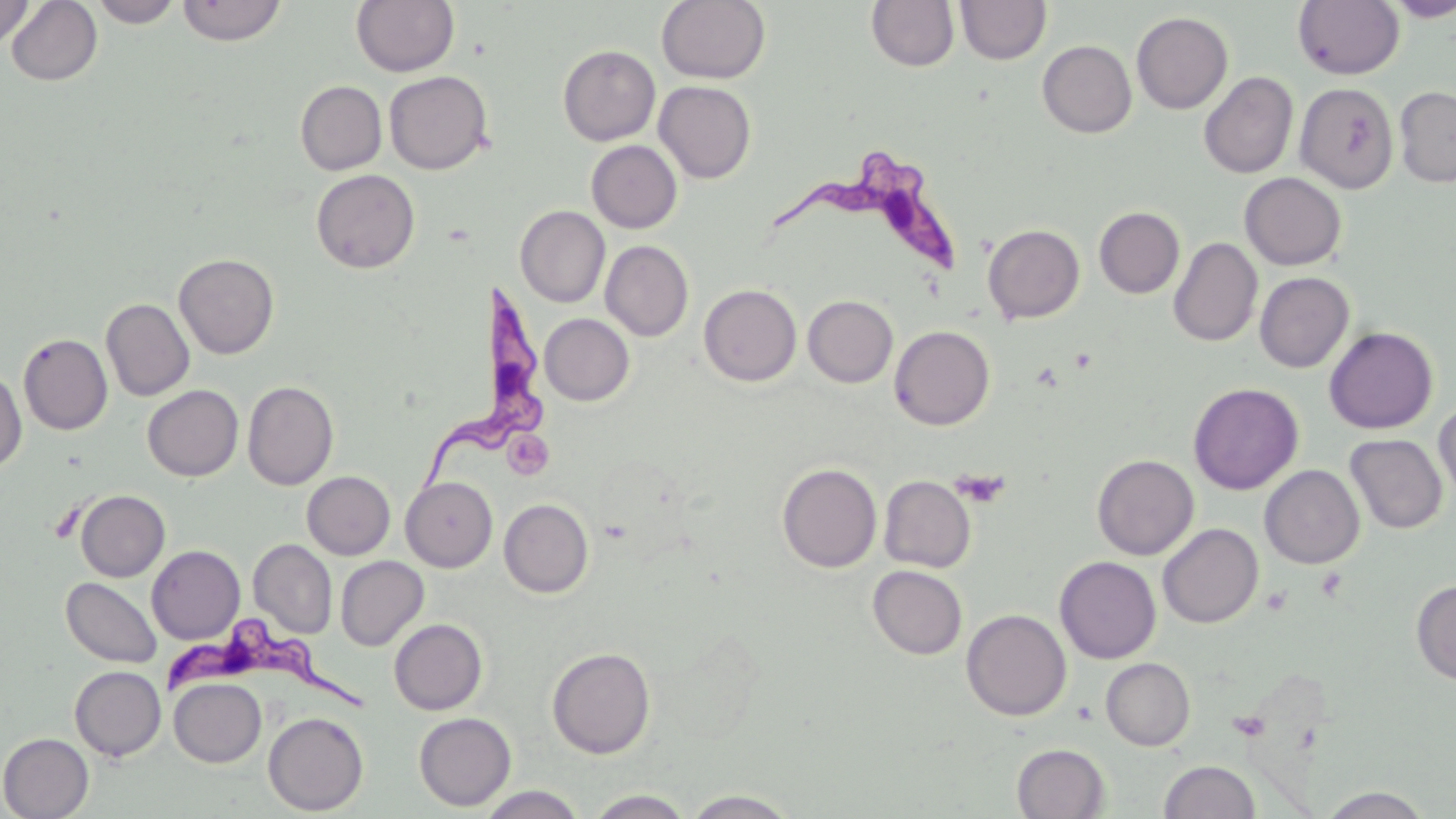
Approximate bounding boxes as (x1,y1)-(x2,y2) corner pairs in pixels. Platelet locations: (507,436)-(555,474), (949,469)-(1011,508). Uninfected red blood cell locations: (90,0)-(182,27), (177,0)-(287,46), (1293,0)-(1405,79), (1382,0)-(1456,21), (0,1)-(34,50), (5,1)-(103,86), (351,1)-(459,77), (656,1)-(771,84), (866,1)-(960,72), (955,1)-(1051,65), (1131,11)-(1233,114), (1037,40)-(1136,137), (558,45)-(660,146), (384,70)-(493,175), (1199,71)-(1298,179), (295,80)-(387,175), (654,81)-(756,183), (1294,82)-(1399,194), (1394,86)-(1456,188), (586,140)-(682,233), (311,169)-(420,274), (1239,172)-(1346,270), (515,205)-(610,307), (1094,206)-(1185,298), (982,224)-(1085,324), (1168,237)-(1262,346), (600,240)-(694,341), (174,253)-(279,359), (1254,272)-(1354,373), (699,284)-(802,386), (803,295)-(898,387), (101,298)-(194,401), (539,314)-(634,405), (889,325)-(995,430), (1324,326)-(1438,433), (18,333)-(112,435), (0,368)-(27,473), (242,380)-(339,490), (1188,382)-(1304,495), (142,385)-(243,481), (1434,400)-(1456,505), (1345,434)-(1448,534), (1092,454)-(1198,560), (777,463)-(882,572), (1260,464)-(1365,568), (302,471)-(395,559), (879,475)-(976,572), (401,477)-(498,572), (75,490)-(170,581), (499,498)-(594,597), (1157,523)-(1263,628), (248,539)-(337,638), (147,545)-(245,644), (335,556)-(428,651), (1054,556)-(1161,663), (868,565)-(967,659), (61,577)-(163,668), (1411,579)-(1456,686), (961,609)-(1072,721), (389,618)-(488,715), (546,647)-(655,758), (1101,657)-(1195,750), (69,665)-(166,761), (169,678)-(266,767), (263,712)-(368,815), (414,712)-(516,810), (0,733)-(94,818), (1012,743)-(1109,819), (1159,760)-(1261,818), (477,785)-(586,819), (1318,786)-(1436,818), (683,789)-(800,818), (584,790)-(696,818). Trypanosoma brucei locations: (776,152)-(964,278), (425,277)-(544,489), (164,620)-(366,711). Slide-level diagnosis: Trypanosoma brucei. Thin blood smear. Single field of view. Optical microscopy. Image is 1456×819 pixels. May-Grünwald-Giemsa stain. Captured at 1000x magnification.